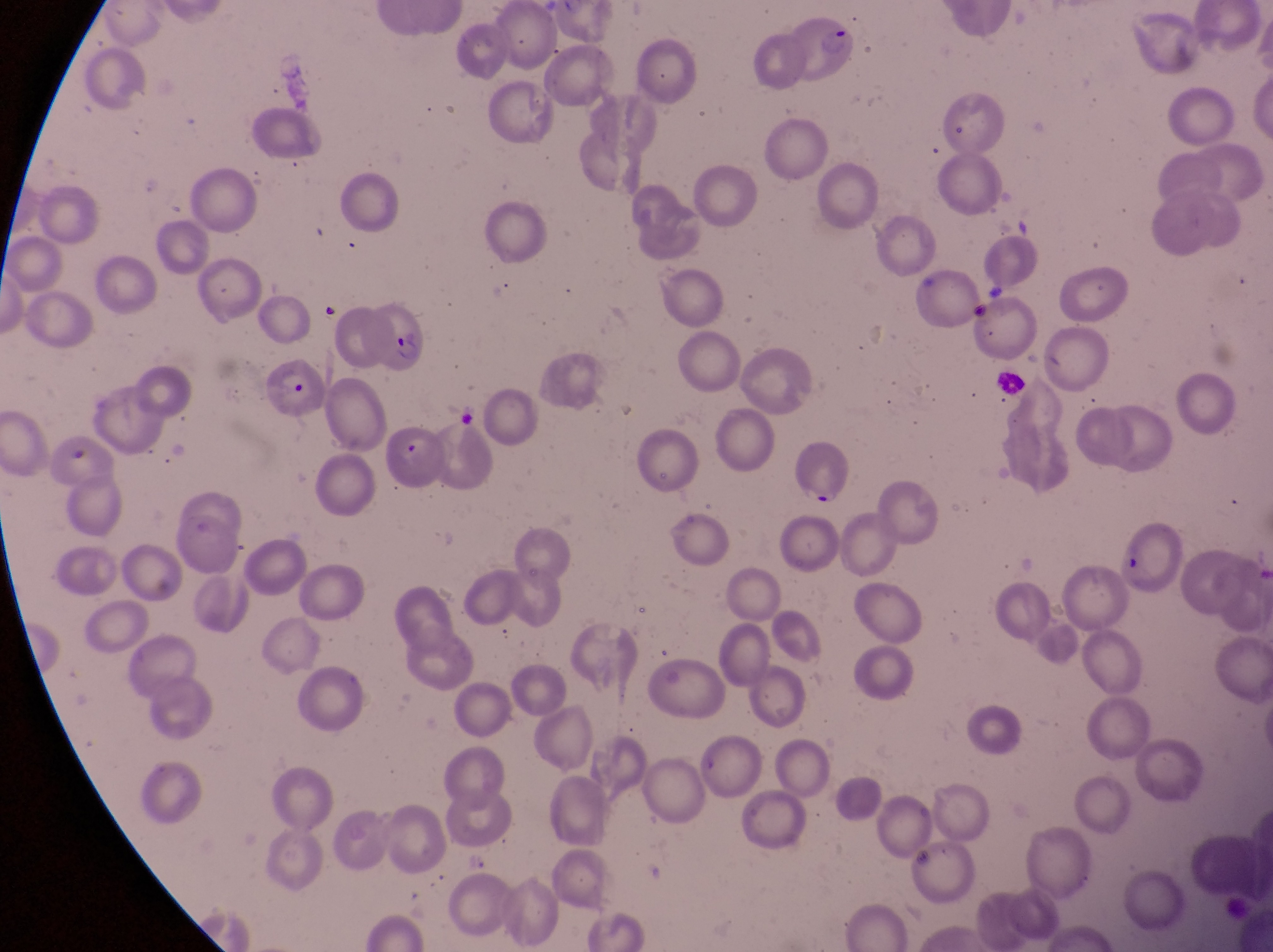

Approximate bounding boxes as left top right bottom in pixels.
Summary:
  - Leukocyte locations: 995 367 1024 400
  - Parasitised red blood cell locations: 356 299 430 374; 257 369 326 427; 799 434 852 508
  - Country: Uganda
  - Magnification: 1000x
  - Field of view: single
  - Capture: smartphone photograph through the eyepiece of an Olympus CX-23 microscope
  - Image size: 1273×952 pixels
  - Preparation: thin blood film